Classify this cell by malaria status.
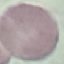
It is uninfected.

stain: Giemsa
image_type: automatically extracted cell patch, resized to 64 × 64 pixels
preparation: thin blood smear
capture: smartphone camera at the microscope eyepiece